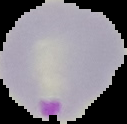
Image is 127×124 pixels. Malaria status: parasitized. Segmented cell region on a black background. From a thin blood smear.